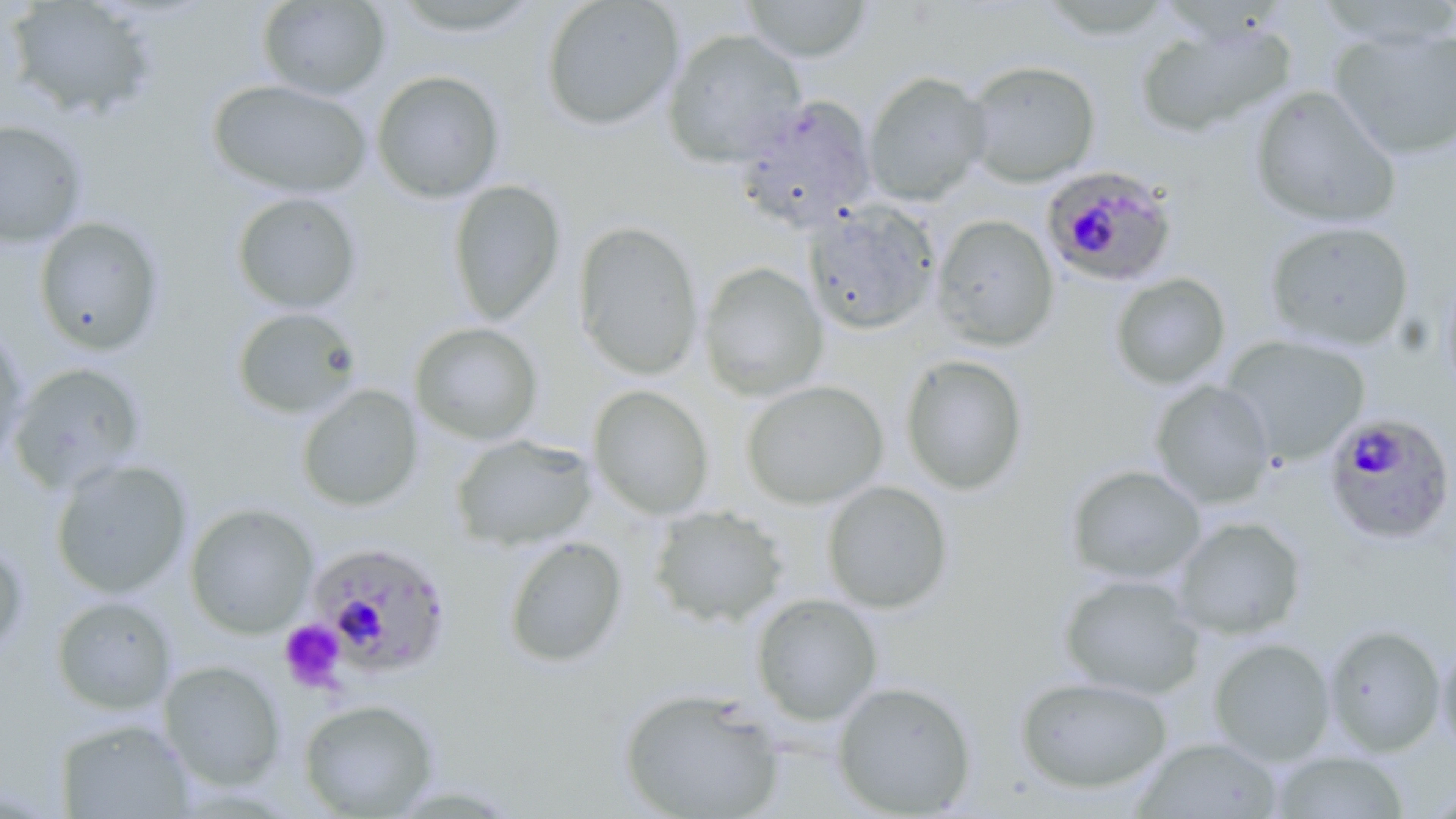

Summary:
  - Coordinate format: approximate bounding boxes as [x1, y1, x2, y2] in pixels
  - Uninfected red blood cell locations: [256, 0, 391, 100], [540, 0, 685, 131], [739, 0, 873, 63], [5, 1, 160, 122], [1312, 1, 1456, 50], [391, 2, 547, 40], [1134, 18, 1296, 139], [1328, 26, 1456, 160], [662, 28, 807, 168], [963, 60, 1101, 188], [371, 69, 505, 204], [863, 71, 992, 207], [207, 79, 373, 200], [1249, 85, 1401, 229], [733, 93, 878, 233], [0, 119, 88, 249], [447, 179, 566, 325], [231, 191, 363, 314], [803, 200, 941, 336], [931, 214, 1059, 351], [32, 215, 166, 356], [1262, 219, 1415, 352], [573, 220, 704, 380], [698, 262, 828, 402], [1439, 263, 1456, 406], [1109, 272, 1231, 390], [231, 306, 363, 421], [409, 322, 543, 446], [0, 325, 30, 471], [1221, 334, 1371, 465], [899, 353, 1030, 496], [8, 362, 148, 495], [740, 379, 889, 510], [1149, 379, 1276, 510], [296, 384, 423, 512], [587, 384, 714, 520], [450, 433, 597, 551], [49, 458, 193, 600], [1065, 464, 1207, 585], [821, 480, 954, 614], [184, 502, 319, 638], [647, 504, 790, 629], [1172, 515, 1308, 640], [502, 535, 628, 669], [0, 537, 29, 663], [1058, 572, 1206, 701], [750, 592, 883, 726], [50, 594, 178, 715], [1323, 624, 1446, 756], [1436, 634, 1456, 760], [1208, 637, 1336, 766], [158, 659, 287, 790], [1015, 675, 1173, 795], [832, 680, 977, 817], [617, 686, 785, 819], [298, 699, 440, 817], [54, 718, 195, 818], [1132, 736, 1285, 818], [1270, 750, 1411, 818]
  - Plasmodium falciparum-infected red blood cell locations: [1041, 165, 1178, 287], [1322, 411, 1456, 546], [307, 541, 453, 679]
  - Platelet locations: [279, 620, 347, 694]
  - Slide-level diagnosis: Plasmodium falciparum
  - Modality: optical microscopy
  - Magnification: 1000x
  - Image size: 1456×819 pixels
  - Preparation: thin blood film
  - Stain: May-Grünwald-Giemsa
  - Field of view: single